Name the parasite shown.
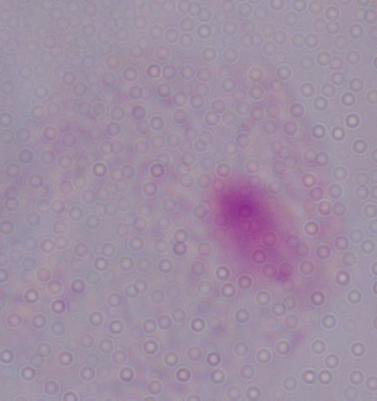

A trichomonad.

Summary:
  - Modality: micrograph
  - Magnification: 1000x